Point out each Plasmodium parasite.
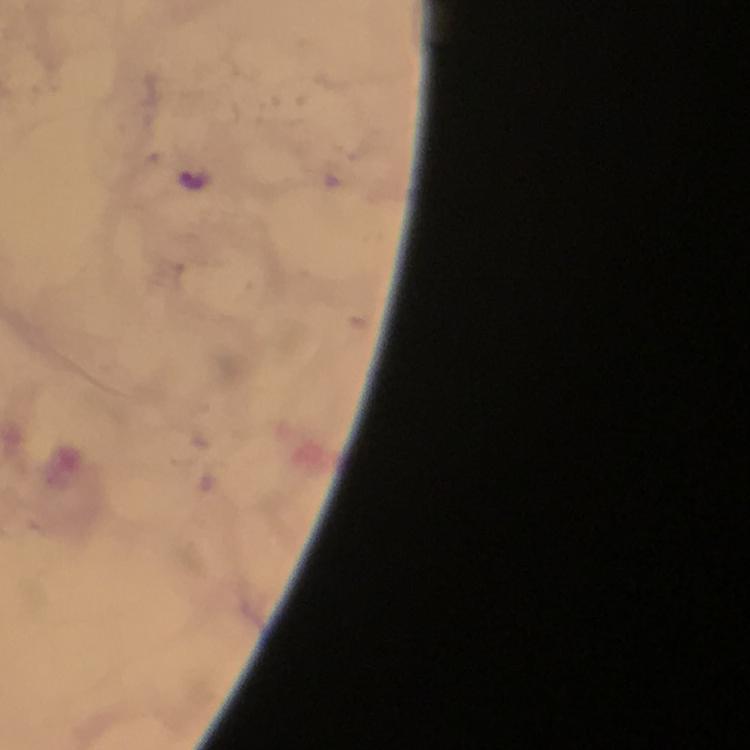
Approximate object centers, in pixels from the top-left corner.
Plasmodium parasites: (x=193, y=178).

Summary:
  - Cropped from: a single field of view
  - Preparation: thick blood smear
  - Context: from a malaria diagnostic workup
  - Magnification: 100x
  - Immersion oil: applied
  - Stain: Giemsa
  - Image size: 750×750 pixels
  - Capture: smartphone camera through the microscope